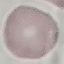
result: no malaria parasites detected
capture: smartphone through the microscope eyepiece
image_type: cell patch, automatically extracted from a larger field of view and resized to 64 × 64 pixels
stain: Giemsa
preparation: thin blood film